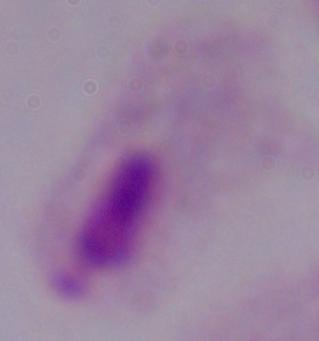

A trichomonad is shown. Captured at 1000x magnification. Micrograph.